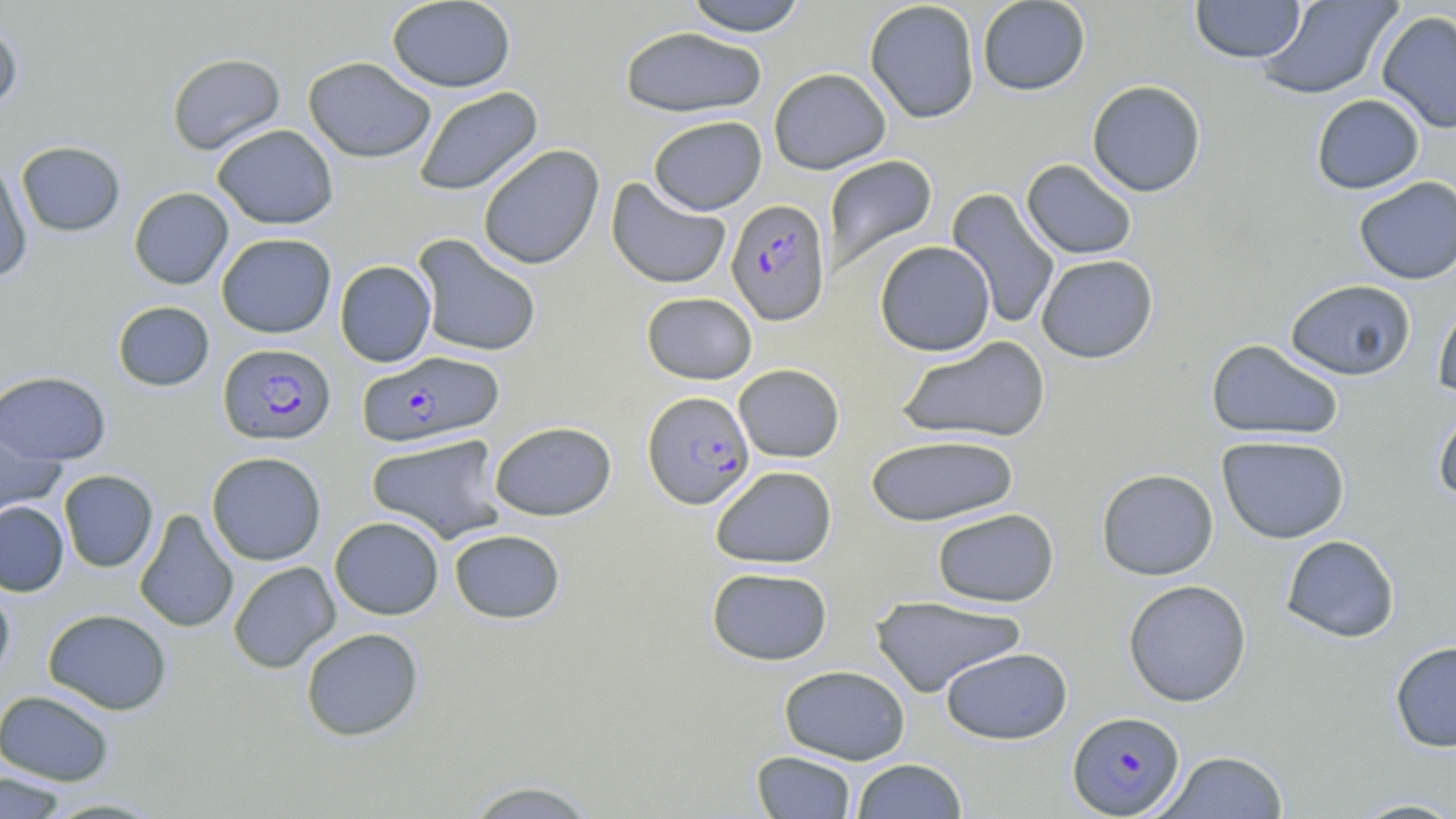
Summary:
  - Coordinate format: approximate bounding boxes as (x1, y1, x2, y2) in pixels
  - Uninfected red blood cell locations: (386, 0, 516, 93), (682, 0, 809, 36), (976, 0, 1091, 96), (1190, 0, 1306, 63), (1256, 0, 1402, 100), (864, 1, 980, 124), (1376, 10, 1456, 134), (0, 18, 23, 114), (620, 26, 767, 118), (166, 52, 285, 155), (303, 56, 436, 163), (768, 67, 891, 175), (1087, 80, 1207, 197), (413, 86, 543, 197), (1311, 94, 1425, 194), (648, 116, 767, 215), (211, 124, 339, 229), (16, 141, 125, 236), (477, 144, 605, 270), (822, 155, 938, 279), (0, 157, 33, 282), (1021, 159, 1137, 260), (1353, 176, 1456, 285), (606, 178, 732, 290), (128, 187, 233, 290), (945, 188, 1061, 331), (216, 233, 336, 338), (412, 233, 542, 358), (874, 240, 995, 356), (1036, 254, 1158, 363), (334, 260, 436, 367), (1285, 279, 1416, 380), (641, 292, 757, 385), (1433, 293, 1456, 401), (112, 300, 215, 392), (895, 336, 1051, 444), (1206, 339, 1345, 441), (733, 364, 845, 463), (0, 371, 111, 465), (1433, 404, 1456, 506), (0, 420, 66, 524), (489, 420, 617, 521), (366, 433, 509, 544), (865, 433, 1019, 526), (1216, 434, 1351, 544), (206, 451, 327, 565), (710, 465, 837, 569), (1096, 468, 1219, 581), (58, 469, 158, 572), (1, 500, 69, 596), (932, 507, 1059, 607), (134, 508, 239, 634), (330, 516, 444, 620), (449, 529, 565, 624), (1281, 535, 1400, 643), (228, 560, 341, 673), (706, 566, 833, 665), (0, 579, 16, 684), (1123, 579, 1252, 707), (869, 595, 1027, 697), (42, 608, 172, 715), (300, 627, 424, 742), (1389, 641, 1456, 753), (940, 646, 1073, 745), (779, 664, 911, 764), (0, 689, 115, 786), (1156, 750, 1290, 818), (752, 751, 857, 818), (850, 758, 968, 818), (0, 772, 70, 819), (461, 779, 602, 819), (37, 796, 169, 818), (1346, 796, 1456, 818)
  - Plasmodium falciparum-infected red blood cell locations: (726, 198, 830, 324), (218, 343, 336, 445), (358, 351, 504, 448), (642, 390, 755, 509), (1067, 710, 1184, 817)
  - Slide-level diagnosis: Plasmodium falciparum
  - Magnification: 1000x
  - Preparation: thin blood smear
  - Modality: light microscopy
  - Stain: May-Grünwald-Giemsa
  - Field of view: one of a larger specimen
  - Image size: 1456×819 pixels